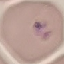
Summary:
  - Malaria status: parasitized
  - Image type: automatically extracted cell patch, resized to 64 × 64 pixels
  - Capture: smartphone camera at the microscope eyepiece
  - Preparation: thin smear
  - Stain: Giemsa